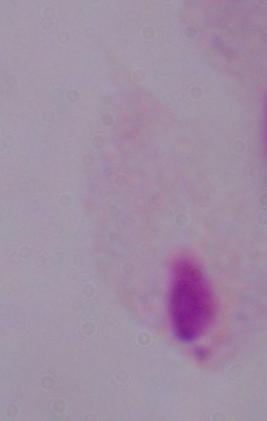
Summary:
  - Magnification: 1000x
  - Identification: trichomonad
  - Modality: photomicrograph